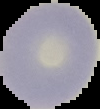

preparation = thin blood smear
image size = 100×109 pixels
image type = segmented cell region on a black background
malaria status = uninfected